Name the parasite shown.
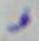
Toxoplasma gondii.

Micrograph. 1000x magnification.